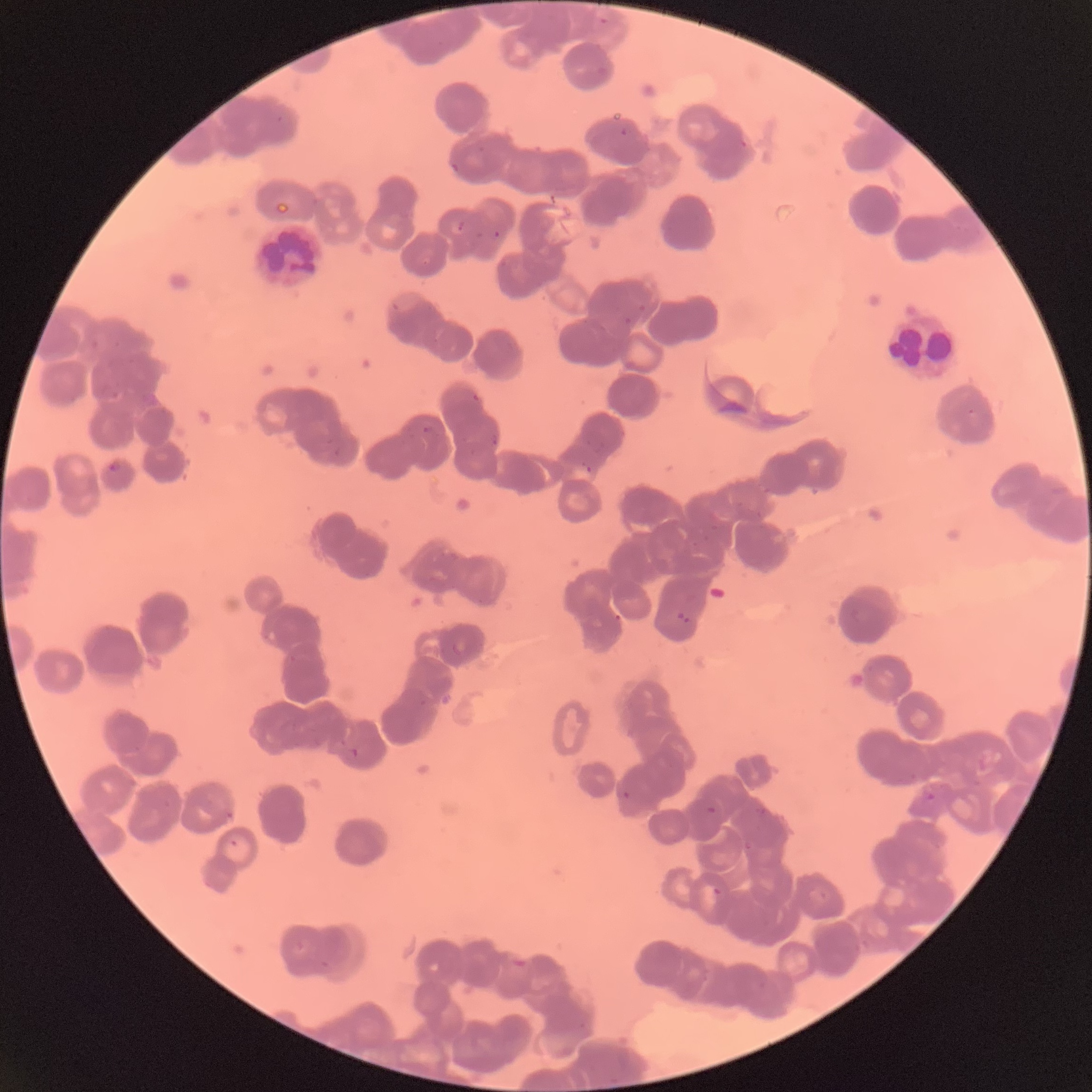

Summary:
  - Coordinate format: approximate bounding boxes as (x1,y1)-(x2,y2) corner pairs in pixels
  - Plasmodium parasite locations: (599,16)-(610,26), (277,115)-(284,123), (620,127)-(630,138), (738,137)-(749,149), (450,162)-(460,174), (457,220)-(465,232), (493,230)-(501,239), (391,302)-(401,312), (636,303)-(646,313), (623,316)-(633,326), (471,392)-(481,402), (718,400)-(748,416), (966,407)-(975,416), (422,425)-(436,435), (490,434)-(500,447), (327,435)-(334,444), (333,446)-(342,456), (107,460)-(120,474), (585,464)-(592,473), (676,610)-(691,624), (452,641)-(469,656), (350,745)-(359,758), (622,790)-(630,800), (924,792)-(936,801), (755,804)-(770,817), (706,806)-(716,814), (225,811)-(234,820), (230,839)-(239,847), (744,841)-(752,850), (712,886)-(722,896)
  - White blood cell locations: (888,312)-(960,378)
  - Modality: optical microscopy
  - Preparation: thin blood smear
  - Image size: 1092×1092 pixels
  - Red blood cell morphology: rouleaux formation